Assess the morphology of the erythrocytes.
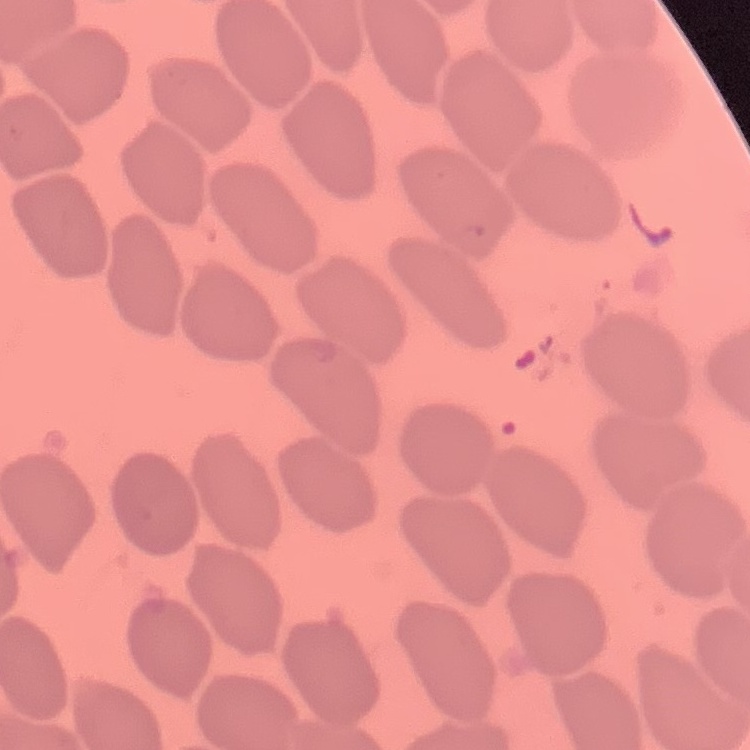
They show no rouleaux formation.

Summary:
  - Image type: square crop of a larger photomicrograph
  - Preparation: thin peripheral smear
  - Stain: Field's or Giemsa